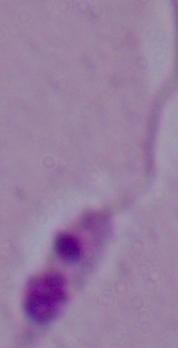
modality = photomicrograph
identification = Leishmania
magnification = 1000x